Locate every Plasmodium falciparum-infected red blood cell.
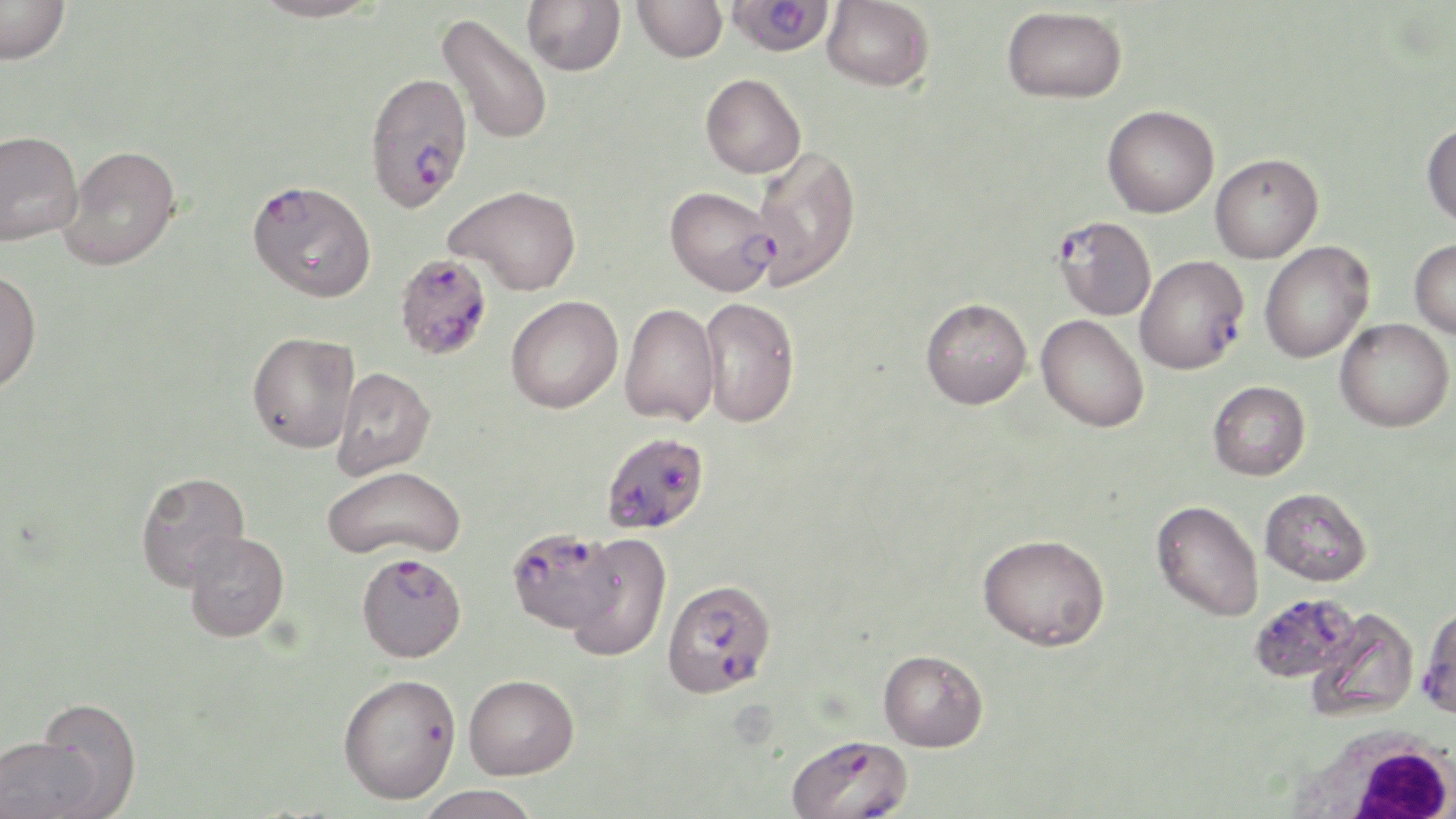
Approximate bounding boxes as [x1, y1, x2, y2] in pixels.
Plasmodium falciparum-infected red blood cells: [725, 0, 835, 57], [364, 71, 473, 213], [247, 179, 377, 303], [665, 185, 779, 296], [1054, 216, 1157, 321], [1136, 255, 1249, 375], [396, 256, 496, 363], [605, 438, 704, 532], [509, 533, 619, 631], [356, 552, 467, 662], [661, 577, 776, 697], [1250, 593, 1361, 685], [1418, 605, 1456, 720], [786, 733, 913, 819].

slide_level_diagnosis: Plasmodium falciparum
field_of_view: single
preparation: thin blood smear
stain: May-Grünwald-Giemsa
uninfected_red_blood_cell_locations: 'approximate bounding boxes as [x1, y1, x2, y2] in pixels: [1, 0, 72, 65], [251, 0, 385, 23], [522, 0, 625, 76], [633, 0, 728, 62], [822, 0, 934, 91], [1002, 6, 1127, 103], [436, 13, 554, 145], [701, 73, 806, 178], [1102, 105, 1219, 218], [1422, 121, 1456, 229], [0, 130, 82, 245], [60, 145, 181, 270], [751, 145, 862, 290], [1210, 153, 1323, 263], [447, 184, 581, 295], [1410, 239, 1456, 339], [1259, 241, 1374, 363], [0, 270, 42, 394], [506, 295, 623, 413], [700, 296, 800, 428], [920, 297, 1032, 409], [619, 303, 720, 427], [1037, 314, 1149, 432], [1335, 318, 1454, 432], [247, 331, 361, 453], [329, 367, 436, 479], [1208, 381, 1310, 480], [321, 464, 467, 561], [135, 471, 250, 591], [1260, 487, 1372, 586], [1151, 501, 1265, 622], [183, 531, 290, 642], [566, 533, 672, 661], [977, 533, 1110, 651], [1307, 607, 1419, 722], [878, 649, 988, 752], [338, 673, 462, 804], [463, 673, 579, 779], [32, 698, 143, 817], [0, 734, 102, 819], [415, 785, 543, 819]'
modality: light microscopy
magnification: 1000x
image_size: 1456×819 pixels
white_blood_cell_locations: 'approximate bounding boxes as [x1, y1, x2, y2] in pixels: [1289, 722, 1455, 819]'